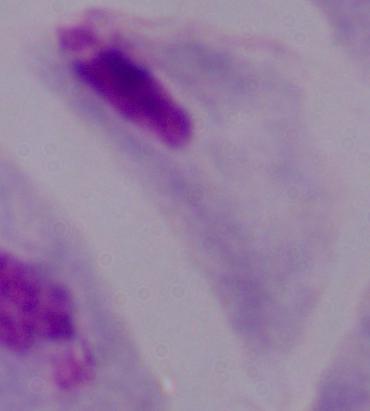
modality = photomicrograph
identification = trichomonad
magnification = 1000x